Give the position of every Plasmodium parasite.
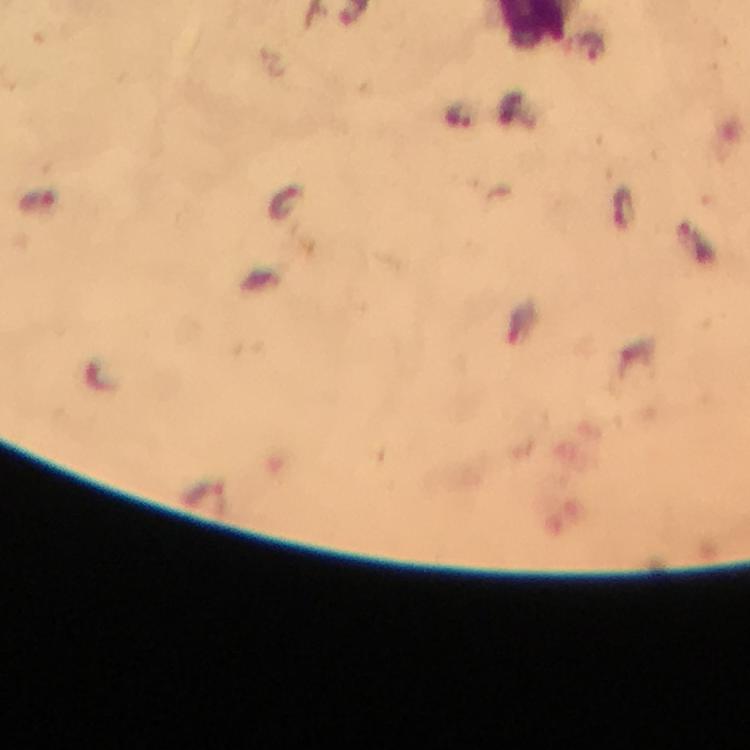
Approximate centers as [x, y] in pixels.
Plasmodium parasites: [593, 48], [460, 117].

Summary:
  - Image size: 750×750 pixels
  - Stain: Giemsa
  - Preparation: thick blood film
  - Magnification: 100x
  - Cropped from: one field of view
  - Immersion oil: applied
  - Capture: smartphone camera through the microscope
  - Context: from a malaria diagnostic workup